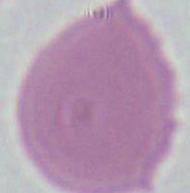 A red blood cell is shown. Micrograph. 1000x magnification.